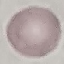
Result: negative for malaria parasites. Thin smear of blood. Cell patch, automatically extracted from a larger field of view and resized to 64 × 64 pixels. Photographed with a smartphone camera at the microscope eyepiece. Giemsa-stained preparation.